Comment on the morphology of the erythrocytes.
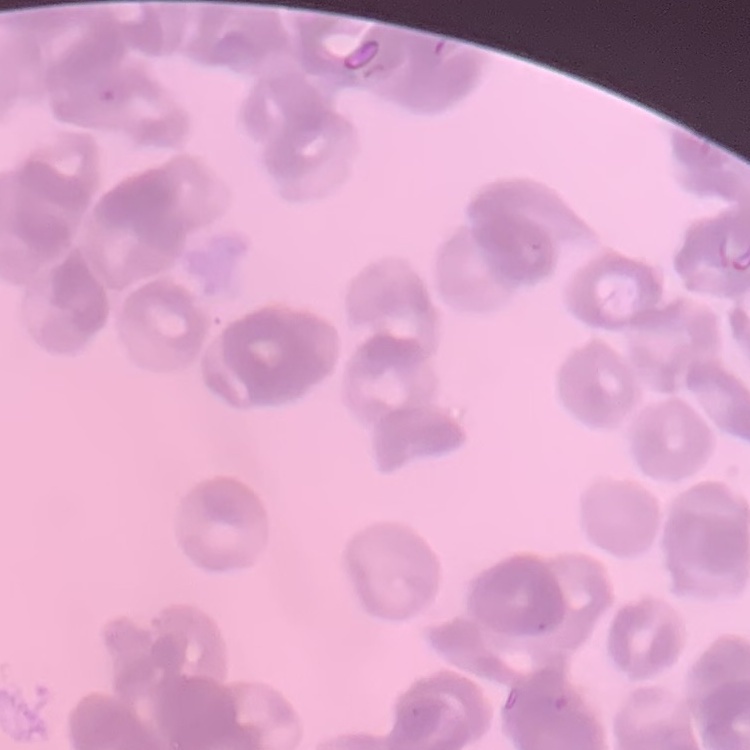

They show rouleaux formation.

One tile cut from a larger photomicrograph. Thin peripheral smear. Field's or Giemsa stain.